Locate every Plasmodium parasite.
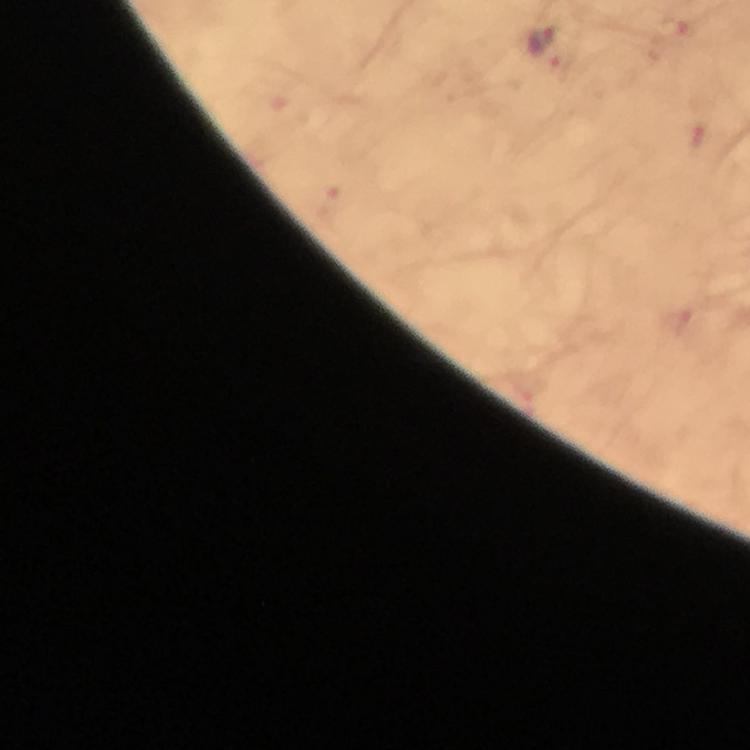

Approximate centers as (x, y) in pixels.
Plasmodium parasites: (669, 30), (542, 37), (563, 60).

context = from a malaria diagnostic workup
image size = 750×750 pixels
preparation = thick smear
magnification = 100x
capture = smartphone mounted on the microscope
stain = Giemsa
cropped from = a single field of view
immersion oil = used